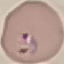
malaria status = parasitized
capture = smartphone through the microscope eyepiece
image type = automatically extracted cell patch, resized to 64 × 64 pixels
preparation = thin blood smear
stain = Giemsa